Name the parasite shown.
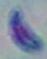

Toxoplasma gondii.

1000x magnification. Micrograph.